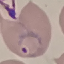
Result: malaria parasites detected. Thin blood smear. Automatically extracted cell patch, resized to 64 × 64 pixels. Acquired by smartphone through the microscope eyepiece. Giemsa-stained preparation.